Give the position of every P. falciparum parasite, noting its life-cycle stage.
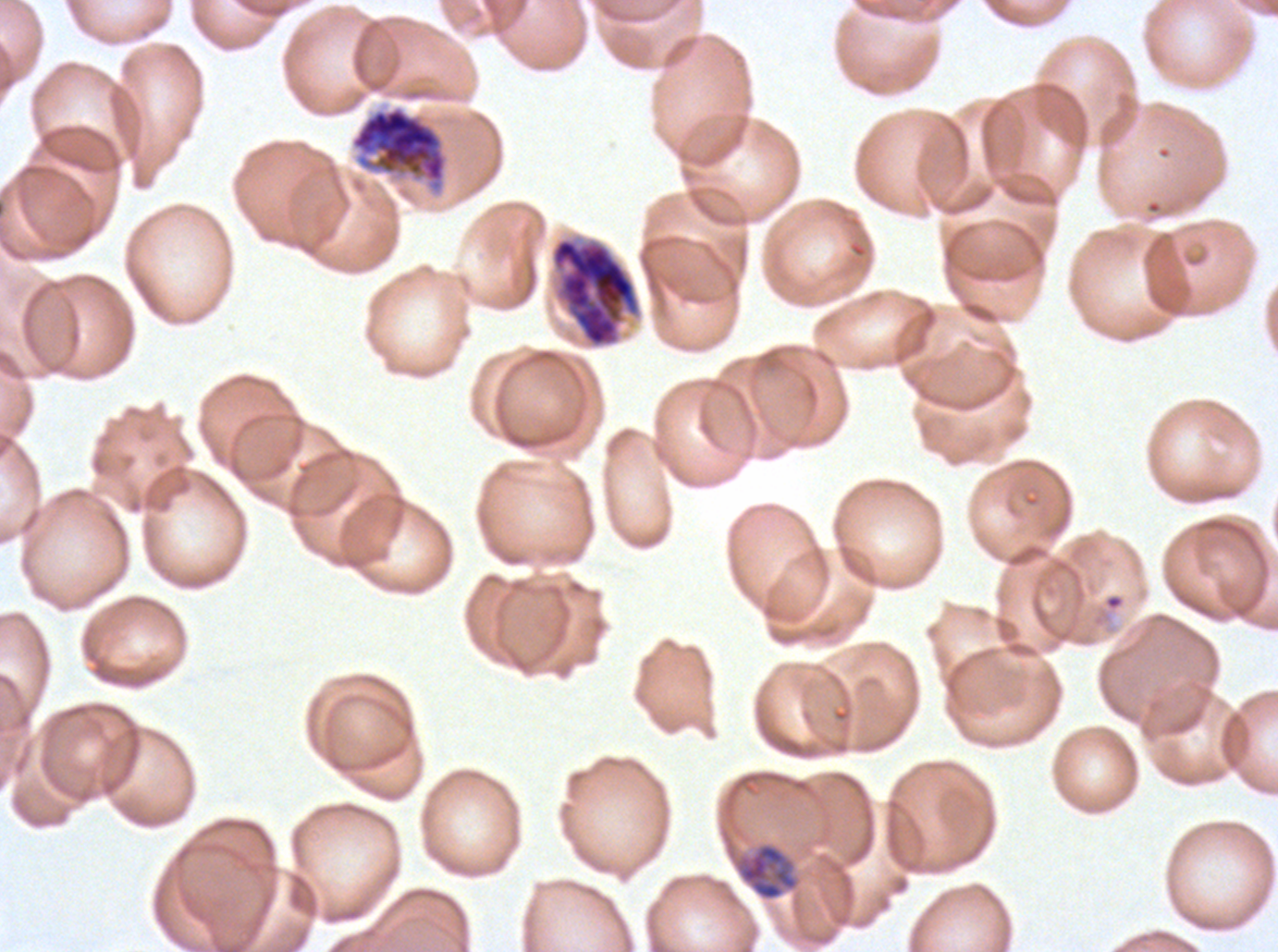

Approximate bounding boxes as [x1, y1, x2, y2] in pixels.
Late-ring/early-trophozoite forms: [1104, 593, 1124, 610].
Mid trophozoites: [733, 841, 800, 901].
Late schizonts: [350, 104, 449, 195], [549, 234, 644, 349].
No rings, late trophozoites, early schizonts, segmenters, or gametocytes observed.

stain = Giemsa
preparation = thin blood film
specimen = P. falciparum from a patient in The Gambia, cultured ex vivo for 24 to 48 hours
field of view = sub-image separated from a larger composite
life-cycle stages observed = late-ring/early-trophozoite, mid trophozoite, late schizont
image size = 1278×952 pixels